Report the malaria status of this cell.
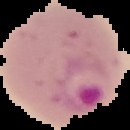
It is parasitized.

Segmented cell region on a black background. Image is 130×130 pixels. From a thin blood film.